Locate every Plasmodium parasite.
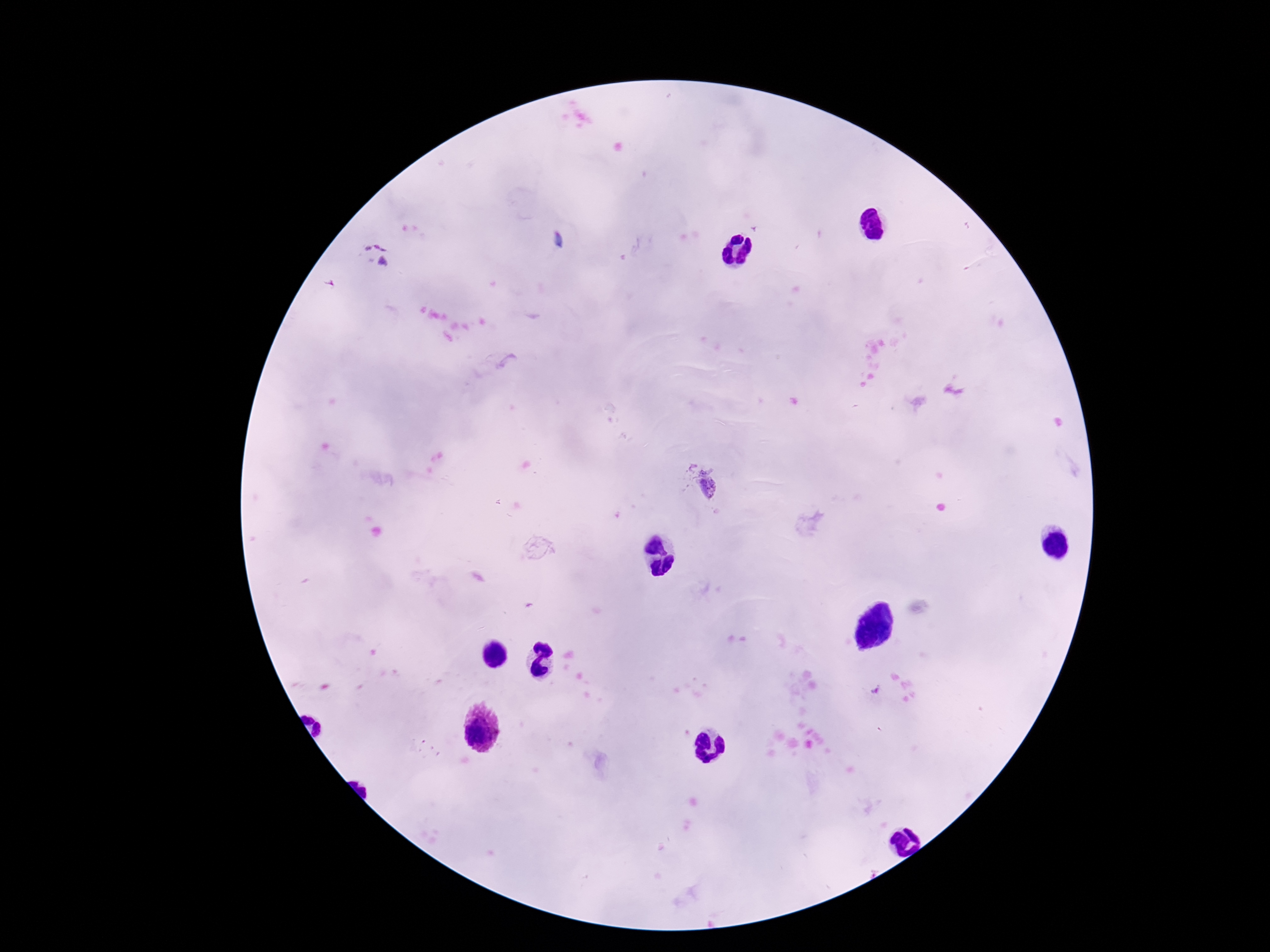
Approximate centers as [x, y] in pixels.
Plasmodium parasites: [375, 254], [698, 484].

100x magnification. Photographed through the microscope eyepiece with a smartphone camera. One field from this slide. Giemsa-stained preparation. Patient malaria status: positive. Image is 1270×952 pixels. Thick blood film.